Assess this cell for malaria.
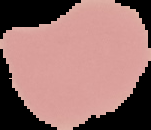

It is uninfected.

preparation = thin blood smear
image type = segmented cell region with the area outside set to black
image size = 151×130 pixels